Name the parasite shown.
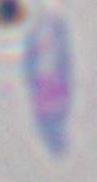

This is Toxoplasma gondii.

Micrograph. 1000x magnification.